Assess for Plasmodium parasites.
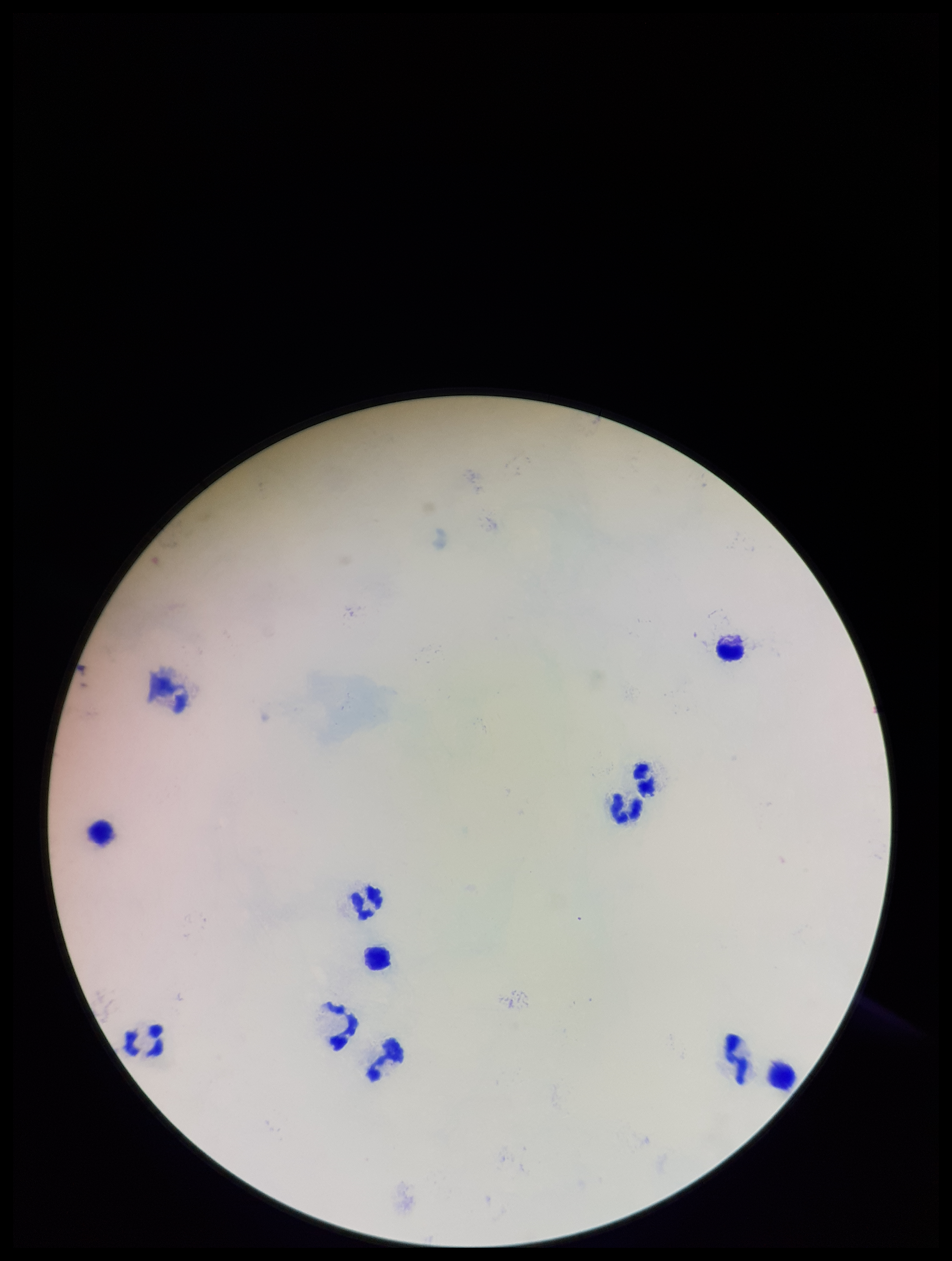

None seen.

Giemsa stain. Photographed through the microscope eyepiece with a smartphone camera. Parasite count: 0. One field from this slide. Leukocyte count: 11. Patient malaria status: negative. Preparation: thick smear. Image is 952×1261 pixels.